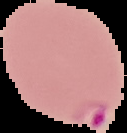

preparation = thin blood film
image type = segmented cell region with the area outside set to black
image size = 127×133 pixels
result = Plasmodium parasites identified